Give the position of every leukocyte visible.
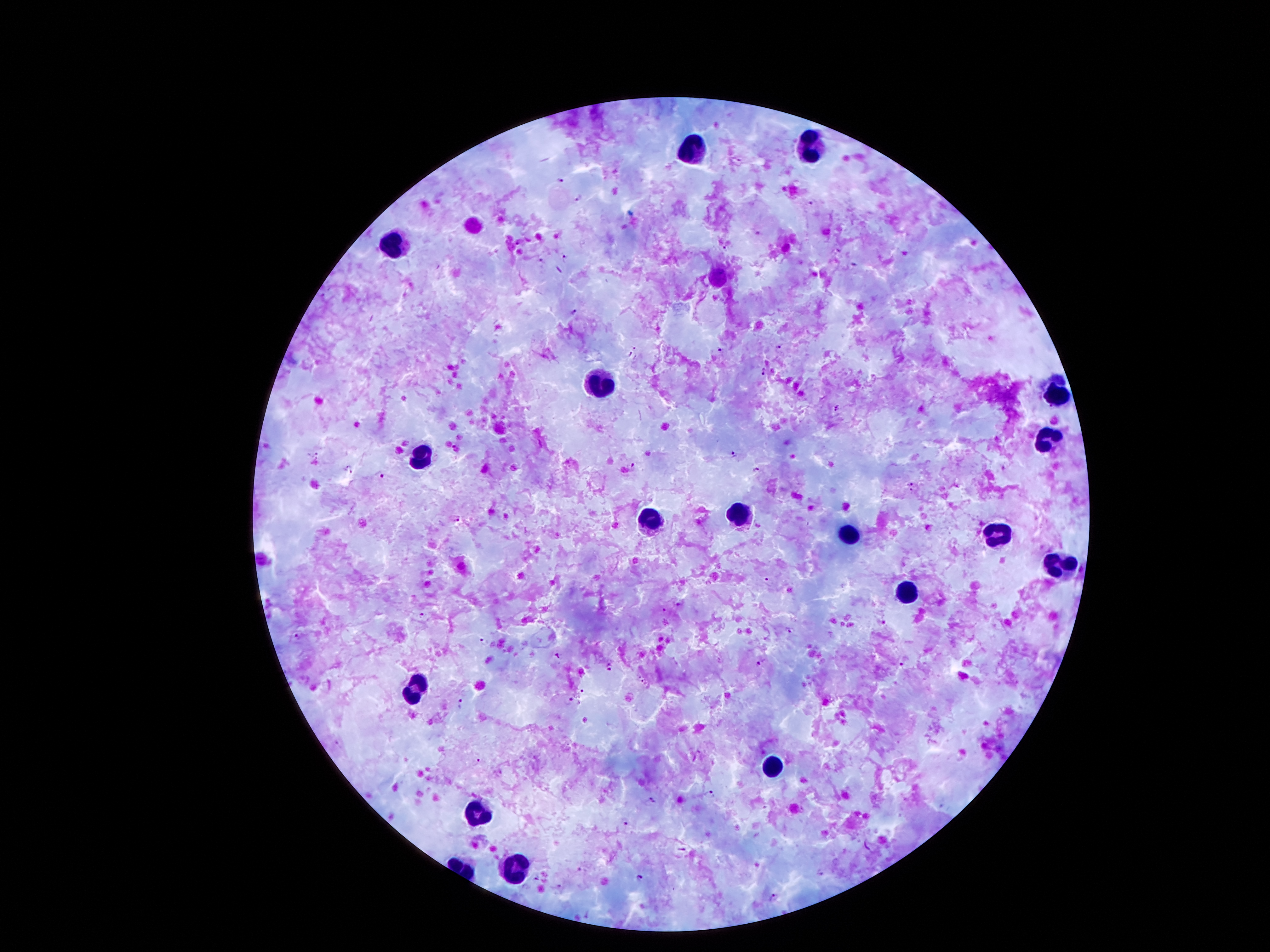

Approximate object centers, in pixels from the top-left corner.
Leukocytes: (x=809, y=148), (x=690, y=150), (x=394, y=241), (x=599, y=383), (x=1057, y=393), (x=1047, y=439), (x=422, y=453), (x=741, y=512), (x=648, y=521), (x=996, y=533), (x=849, y=535), (x=1057, y=563), (x=907, y=591), (x=417, y=691), (x=772, y=764), (x=478, y=813), (x=513, y=864).

Plasmodium parasite locations: (x=559, y=181), (x=579, y=198), (x=811, y=202), (x=726, y=248), (x=563, y=257), (x=540, y=258), (x=575, y=311), (x=779, y=345), (x=720, y=350), (x=632, y=356), (x=764, y=373), (x=837, y=408), (x=456, y=448), (x=733, y=454), (x=315, y=455), (x=632, y=465), (x=348, y=468), (x=757, y=468), (x=380, y=475), (x=912, y=483), (x=911, y=492), (x=457, y=518), (x=767, y=578), (x=680, y=603), (x=665, y=609), (x=421, y=614), (x=791, y=631), (x=298, y=636), (x=485, y=642), (x=557, y=655), (x=762, y=660), (x=902, y=664), (x=610, y=668), (x=642, y=681), (x=582, y=690), (x=571, y=700), (x=460, y=701), (x=585, y=719), (x=477, y=762), (x=710, y=794), (x=652, y=800), (x=626, y=822), (x=682, y=851), (x=581, y=869), (x=819, y=874), (x=537, y=877), (x=640, y=877), (x=557, y=887), (x=526, y=888), (x=774, y=897). Image is 1270×952 pixels. Patient malaria status: infected with Plasmodium falciparum. Smartphone photograph taken through the microscope eyepiece. Giemsa stain. Thick blood smear. 100x magnification. One field from this slide.